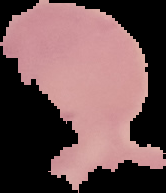
Summary:
  - Image size: 166×193 pixels
  - Image type: segmented cell region on a black background
  - Malaria status: uninfected
  - Preparation: thin blood smear